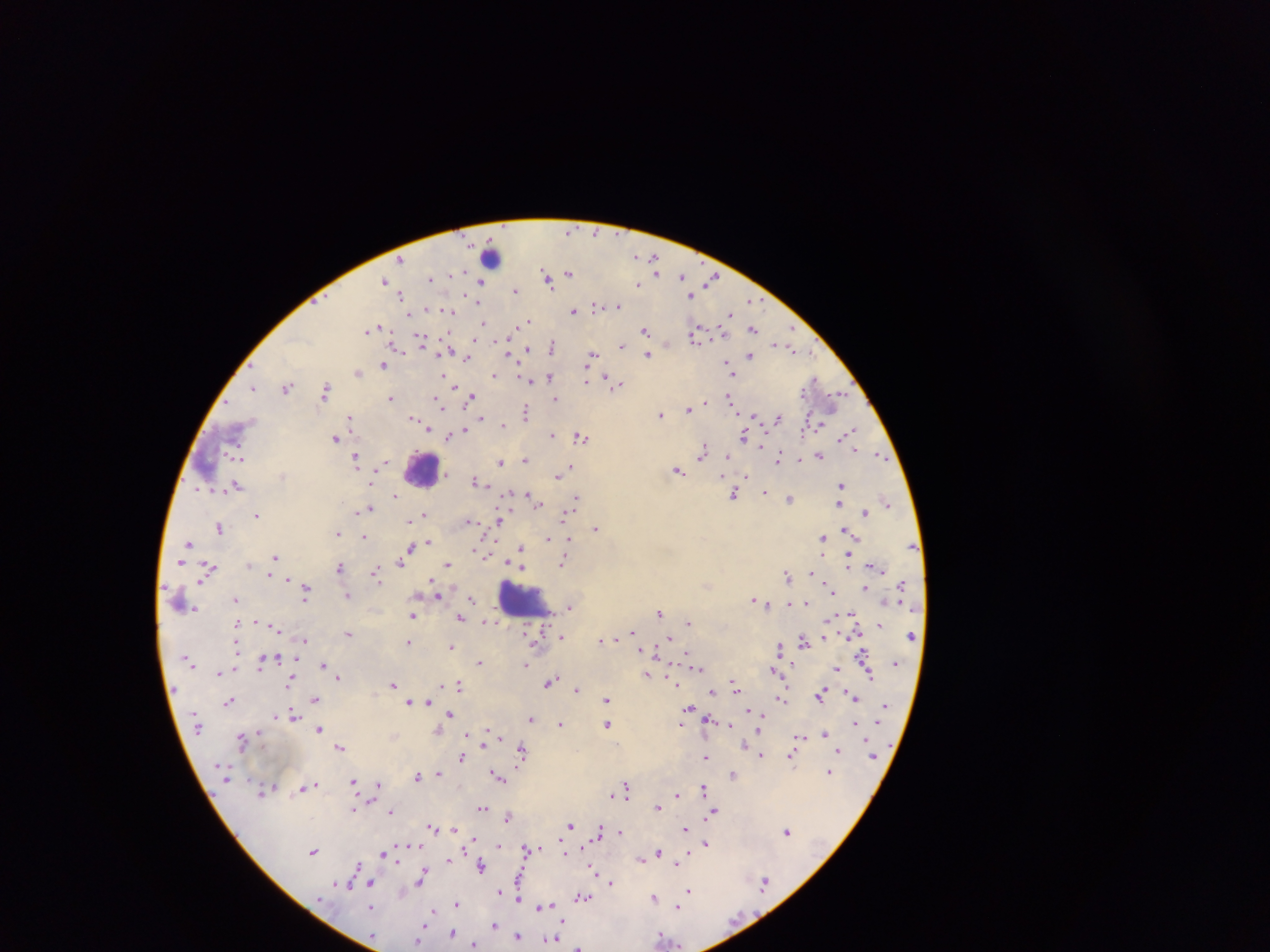
Approximate centers as [x, y] in pixels.
Summary:
  - Leukocyte locations: [490, 257], [422, 470], [183, 599], [522, 599]
  - Plasmodium parasite locations: [570, 231], [637, 257], [654, 259], [401, 260], [657, 271], [570, 273], [545, 274], [452, 276], [682, 276], [431, 279], [712, 279], [548, 280], [384, 281], [480, 282], [637, 284], [515, 290], [401, 295], [691, 295], [750, 300], [596, 306], [618, 306], [607, 307], [573, 311], [410, 313], [450, 313], [729, 314], [528, 320], [484, 325], [372, 328], [645, 329], [753, 329], [792, 329], [481, 332], [696, 334], [422, 341], [666, 344], [621, 345], [527, 348], [552, 348], [791, 348], [509, 354], [592, 354], [647, 355], [750, 355], [467, 357], [727, 363], [383, 365], [357, 372], [729, 372], [444, 376], [494, 376], [549, 376], [814, 379], [528, 380], [586, 380], [616, 384], [452, 385], [253, 387], [287, 387], [326, 390], [470, 397], [729, 397], [391, 398], [837, 398], [555, 399], [439, 403], [689, 409], [526, 412], [660, 415], [754, 416], [350, 418], [481, 418], [777, 418], [415, 419], [423, 423], [503, 426], [463, 431], [849, 432], [552, 435], [744, 435], [448, 436], [581, 436], [335, 439], [761, 445], [703, 453], [238, 455], [818, 456], [728, 457], [779, 457], [881, 457], [357, 458], [800, 459], [525, 460], [500, 461], [570, 467], [678, 471], [558, 476], [476, 481], [841, 485], [236, 486], [765, 492], [735, 494], [395, 495], [529, 497], [577, 497], [790, 498], [536, 502], [887, 502], [839, 504], [369, 508], [570, 510], [865, 513], [425, 514], [256, 515], [565, 515], [411, 521], [469, 521], [498, 521], [219, 528], [596, 528], [848, 531], [338, 533], [363, 537], [548, 538], [823, 538], [427, 542], [189, 543], [410, 547], [520, 548], [477, 551], [276, 557], [402, 560], [848, 560], [563, 562], [447, 565], [520, 566], [340, 567], [209, 569], [376, 573], [269, 574], [787, 575], [306, 589], [865, 589], [831, 590], [436, 592], [348, 596], [236, 599], [472, 599], [754, 600], [768, 604], [788, 604], [805, 604], [570, 607], [659, 612], [413, 615], [460, 617], [488, 622], [688, 623], [880, 625], [633, 632], [347, 633], [562, 636], [668, 638], [304, 640], [601, 640], [803, 640], [410, 642], [451, 647], [779, 647], [655, 652], [863, 655], [261, 662], [480, 663], [324, 664], [526, 664], [698, 667], [837, 669], [773, 670], [220, 672], [647, 675], [338, 676], [869, 676], [290, 681], [550, 682], [674, 683], [392, 684], [734, 684], [459, 686], [561, 687], [577, 689], [712, 692], [821, 693], [853, 697], [314, 698], [781, 698], [606, 699], [229, 701], [410, 702], [428, 703], [689, 708], [293, 715], [450, 715], [762, 718], [531, 719], [708, 719], [681, 723], [855, 723], [561, 724], [608, 724], [729, 725], [319, 729], [825, 733], [799, 737], [242, 739], [341, 746], [839, 750], [522, 751], [761, 755], [706, 757], [461, 758], [792, 758], [829, 772], [438, 773], [733, 774], [417, 775], [497, 777], [353, 783], [313, 785], [379, 785], [307, 787], [626, 788], [704, 789], [263, 792], [613, 794], [677, 795], [658, 807], [481, 808], [353, 809], [391, 811], [714, 811], [508, 817], [570, 826], [432, 827], [453, 828], [684, 829], [787, 831], [599, 832], [620, 832], [706, 843], [499, 845], [527, 848], [313, 851], [384, 853], [659, 854], [641, 858], [680, 858], [448, 859], [676, 862], [357, 866], [481, 866], [593, 869], [421, 878], [610, 882], [370, 884], [763, 884], [340, 885], [689, 890], [518, 897], [582, 897], [654, 897], [457, 903], [544, 906], [678, 907], [430, 913], [493, 925], [452, 933], [517, 936], [420, 937], [662, 937], [550, 939], [475, 945], [579, 947]
  - Field of view: single
  - Capture: mobile-phone photograph through a microscope
  - Preparation: thick blood film
  - Image size: 1270×952 pixels
  - Country: Ghana